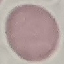

Result: negative for malaria parasites. Giemsa stain. Acquired by smartphone through the microscope eyepiece. Automatically extracted cell patch, resized to 64 × 64 pixels. Thin blood smear.